Assess this cell for malaria.
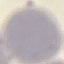
It is uninfected.

Summary:
  - Stain: Giemsa
  - Image type: automatically extracted cell patch, resized to 64 × 64 pixels
  - Capture: smartphone camera at the microscope eyepiece
  - Preparation: thin blood film